Report the malaria status of this cell.
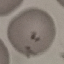
Parasitized.

Photographed with a smartphone camera at the microscope eyepiece. Cell patch, automatically extracted from a larger field of view and resized to 64 × 64 pixels. Thin blood smear. Giemsa-stained preparation.